Classify this cell by malaria status.
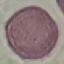

It is uninfected.

stain = Giemsa
capture = smartphone camera at the microscope eyepiece
image type = automatically extracted cell patch, resized to 64 × 64 pixels
preparation = thin blood film